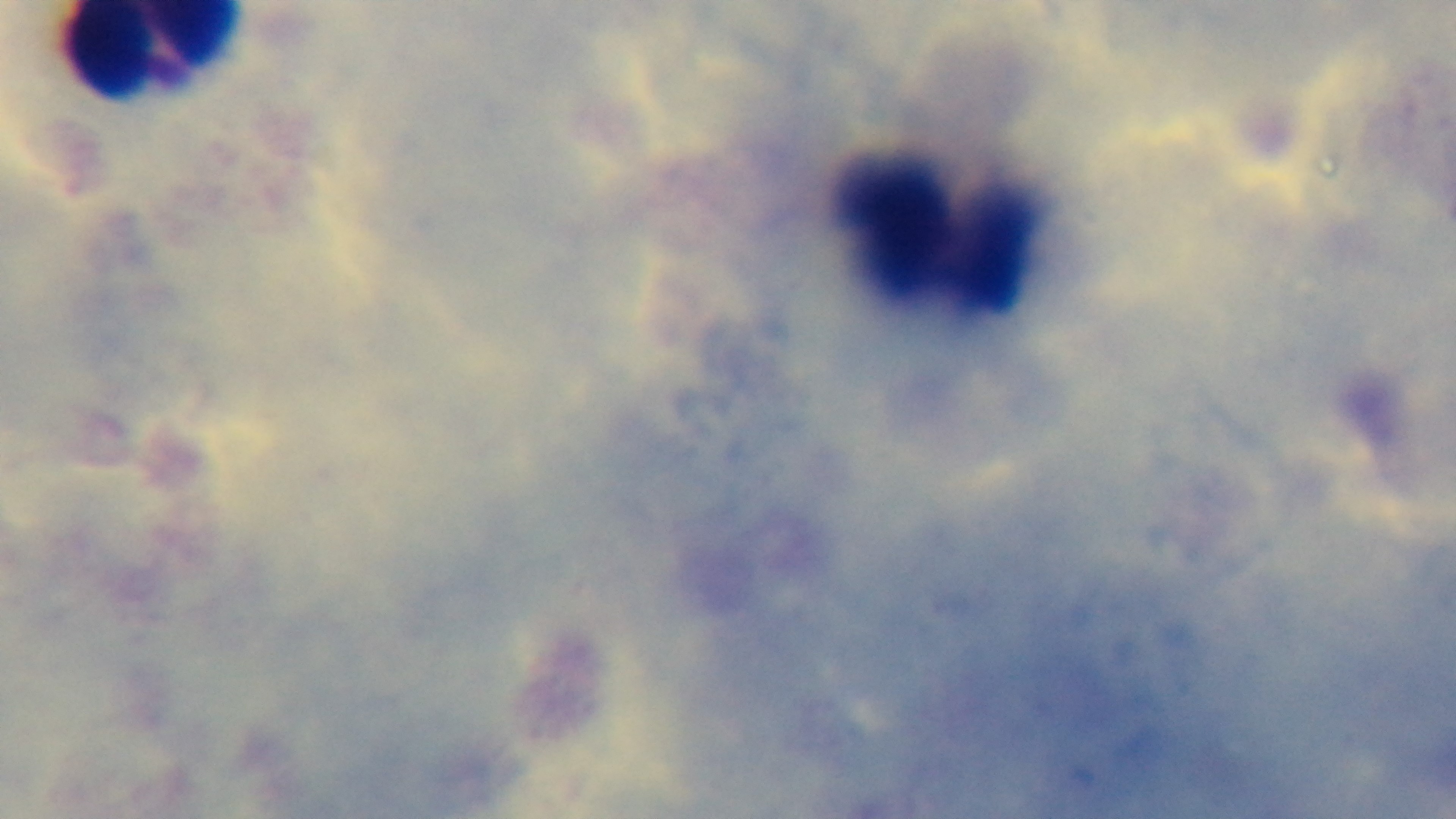
malaria_status: uninfected
objective: 100x oil immersion
capture: mounted 4K digital camera
stain: Giemsa
field_of_view: one from the slide
modality: light microscopy
preparation: thick blood film